State the blood parasite species.
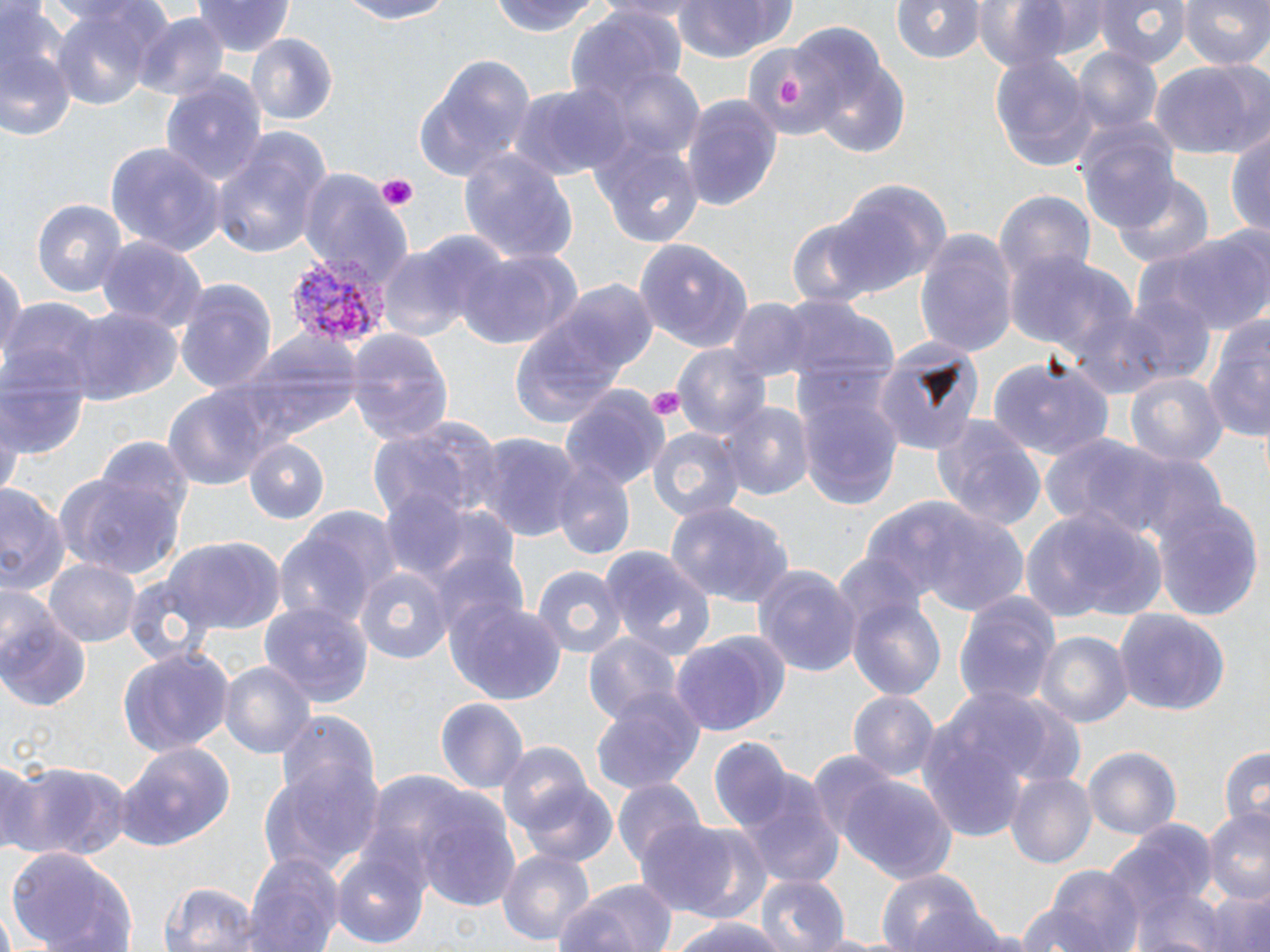
Plasmodium vivax.

Summary:
  - Coordinate format: approximate bounding boxes as [x1, y1, x2, y2] in pixels
  - Platelet locations: [778, 75, 805, 105], [374, 175, 418, 209], [646, 387, 686, 418]
  - Plasmodium vivax-infected red blood cell locations: [287, 254, 389, 348]
  - Uninfected red blood cell locations: [193, 0, 297, 57], [332, 0, 457, 25], [671, 0, 797, 61], [894, 0, 986, 65], [972, 0, 1075, 78], [1091, 0, 1191, 66], [1179, 0, 1269, 71], [484, 2, 613, 38], [47, 5, 166, 115], [1, 7, 77, 143], [566, 11, 685, 112], [134, 15, 229, 103], [245, 32, 337, 126], [739, 39, 837, 141], [1072, 46, 1163, 137], [989, 51, 1096, 170], [811, 54, 910, 158], [416, 56, 537, 179], [1150, 61, 1270, 161], [595, 64, 705, 162], [161, 74, 265, 188], [509, 81, 628, 183], [681, 91, 783, 210], [1074, 118, 1179, 229], [590, 129, 705, 247], [213, 130, 332, 260], [1226, 130, 1270, 241], [105, 143, 225, 262], [457, 148, 581, 265], [300, 169, 408, 286], [1114, 172, 1215, 269], [826, 177, 951, 291], [993, 189, 1095, 288], [34, 199, 127, 300], [1147, 226, 1268, 333], [914, 228, 1017, 358], [637, 234, 749, 354], [93, 237, 206, 335], [377, 245, 471, 343], [451, 246, 578, 354], [0, 252, 24, 374], [1008, 253, 1139, 370], [172, 276, 277, 393], [1115, 290, 1214, 387], [781, 291, 900, 405], [725, 297, 814, 384], [3, 301, 107, 394], [65, 306, 178, 409], [508, 308, 642, 429], [1201, 323, 1270, 452], [213, 327, 363, 451], [347, 329, 456, 446], [870, 335, 984, 455], [674, 344, 772, 443], [0, 351, 91, 462], [989, 355, 1114, 458], [1125, 371, 1227, 470], [797, 384, 902, 511], [163, 386, 272, 495], [559, 387, 671, 490], [717, 401, 813, 500], [930, 412, 1046, 533], [2, 414, 19, 502], [368, 418, 496, 521], [646, 426, 743, 522], [1037, 431, 1202, 548], [476, 433, 580, 541], [92, 438, 194, 544], [245, 439, 331, 525], [551, 467, 635, 560], [58, 472, 186, 579], [0, 483, 67, 598], [379, 489, 471, 582], [869, 498, 1036, 620], [1154, 500, 1264, 618], [665, 501, 796, 610], [1021, 504, 1162, 624], [275, 533, 376, 630], [153, 539, 288, 635], [600, 545, 716, 661], [430, 546, 532, 647], [43, 557, 141, 647], [752, 564, 864, 677], [531, 565, 627, 662], [354, 566, 454, 668], [954, 588, 1062, 710], [845, 590, 948, 706], [446, 599, 566, 705], [259, 600, 374, 707], [1114, 608, 1229, 716], [1, 611, 90, 711], [582, 631, 683, 727], [669, 631, 790, 736], [1037, 631, 1132, 729], [119, 649, 234, 756], [218, 661, 314, 761], [913, 686, 1063, 840], [590, 690, 705, 794], [848, 690, 940, 785], [435, 697, 529, 794], [276, 710, 377, 807], [707, 734, 807, 844], [115, 740, 237, 853], [497, 743, 596, 836], [1084, 746, 1182, 840], [1216, 746, 1269, 833], [806, 753, 898, 851], [261, 754, 384, 874], [0, 759, 47, 855], [14, 763, 133, 860], [1005, 771, 1095, 869], [733, 772, 843, 887], [837, 774, 959, 886], [513, 778, 620, 868], [613, 778, 706, 868], [413, 790, 525, 913], [1203, 806, 1270, 900], [1102, 820, 1214, 948], [635, 821, 753, 915], [330, 843, 431, 948], [6, 848, 135, 952], [497, 848, 596, 950], [243, 850, 344, 952], [1037, 865, 1144, 952], [878, 870, 988, 952], [753, 873, 848, 952], [556, 877, 680, 952], [162, 882, 264, 952], [1195, 885, 1270, 952], [670, 916, 787, 952], [804, 932, 896, 951]
  - Modality: light microscopy
  - Image size: 1270×952 pixels
  - Preparation: thin blood film
  - Field of view: one of a larger specimen
  - Magnification: 1000x
  - Stain: May-Grünwald-Giemsa